Give the position of every Plasmodium parasite.
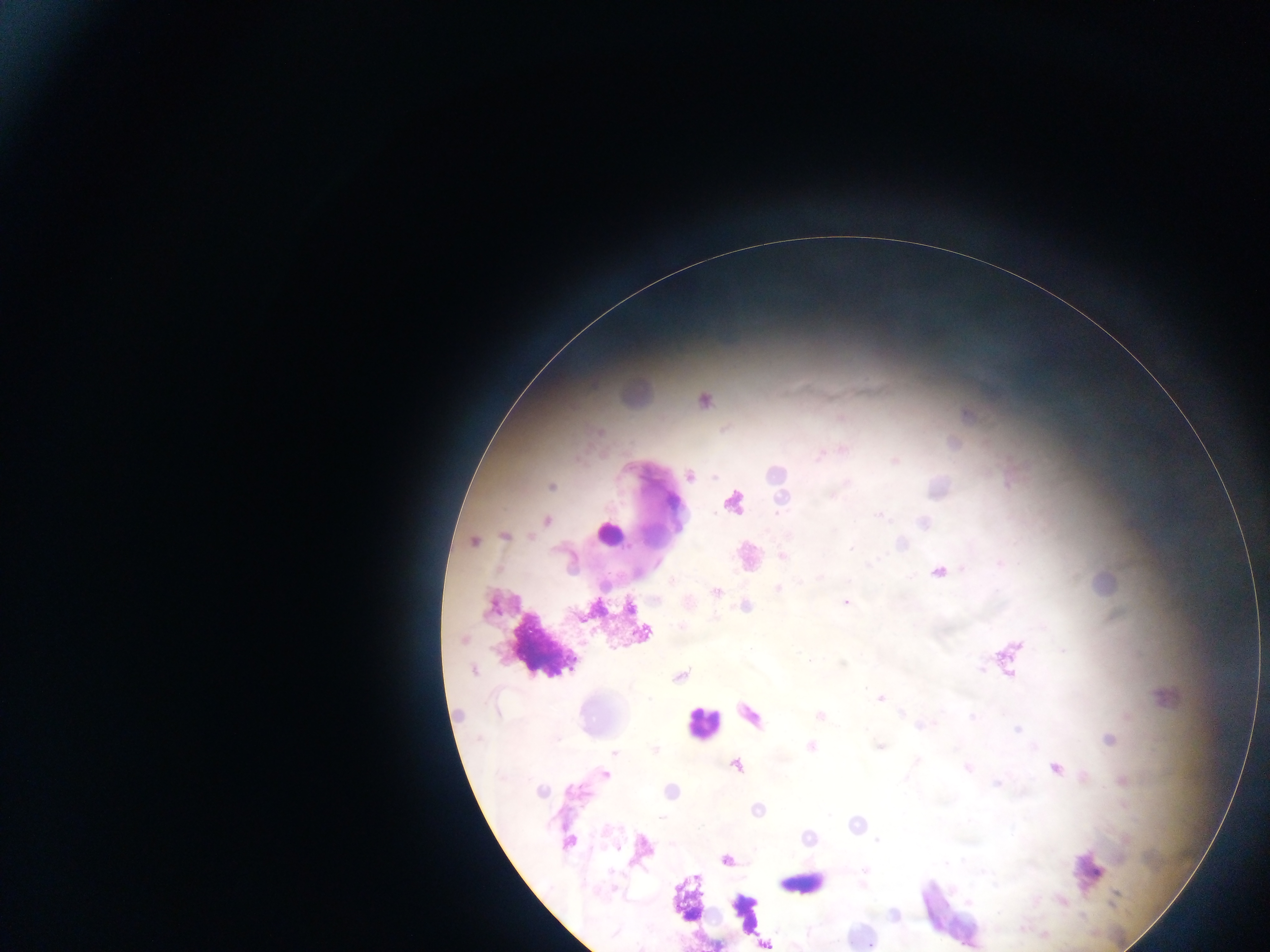

Approximate centers as x y in pixels.
Plasmodium parasites: 704 401; 954 444; 820 455; 895 461; 690 476; 551 487; 781 499; 732 502; 879 515; 547 520; 505 536; 474 542; 851 549; 782 556; 939 572; 779 589; 716 592; 846 602; 629 608; 644 633; 463 640; 1009 657; 473 670; 680 676; 881 698; 820 716; 1017 730; 1109 740; 811 746; 655 749; 615 752; 737 766; 968 768; 1054 769; 605 775; 877 841; 568 843; 727 860; 967 901; 765 944.

Summary:
  - Leukocyte locations: 635 391; 610 533; 750 556; 1105 584; 700 723; 805 882
  - Image size: 1270×952 pixels
  - Field of view: single
  - Preparation: thick blood smear
  - Capture: mobile-phone photograph through a microscope
  - Country: Ghana